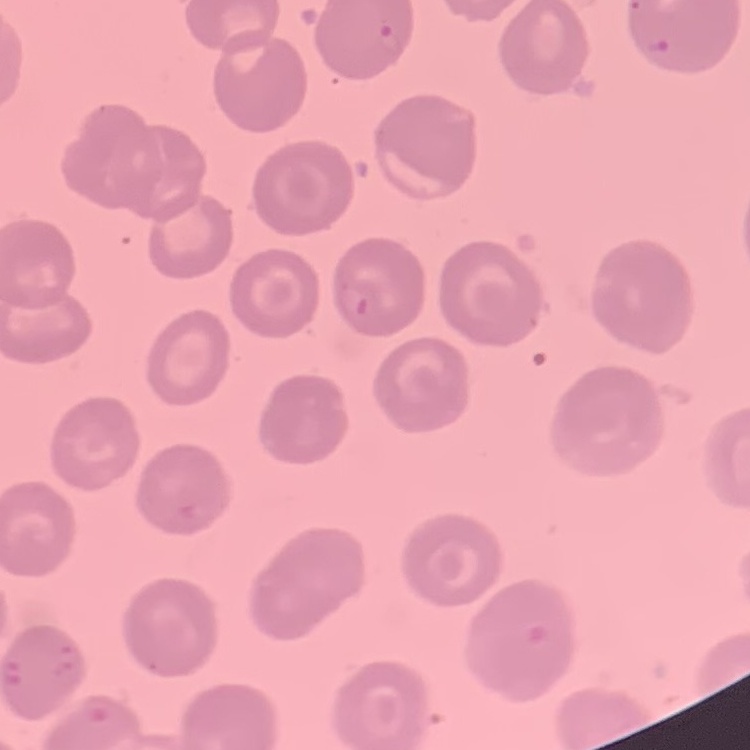

Summary:
  - Red blood cell morphology: no rouleaux formation
  - Stain: Field's or Giemsa
  - Preparation: thin blood film
  - Image type: one tile cut from a larger photomicrograph